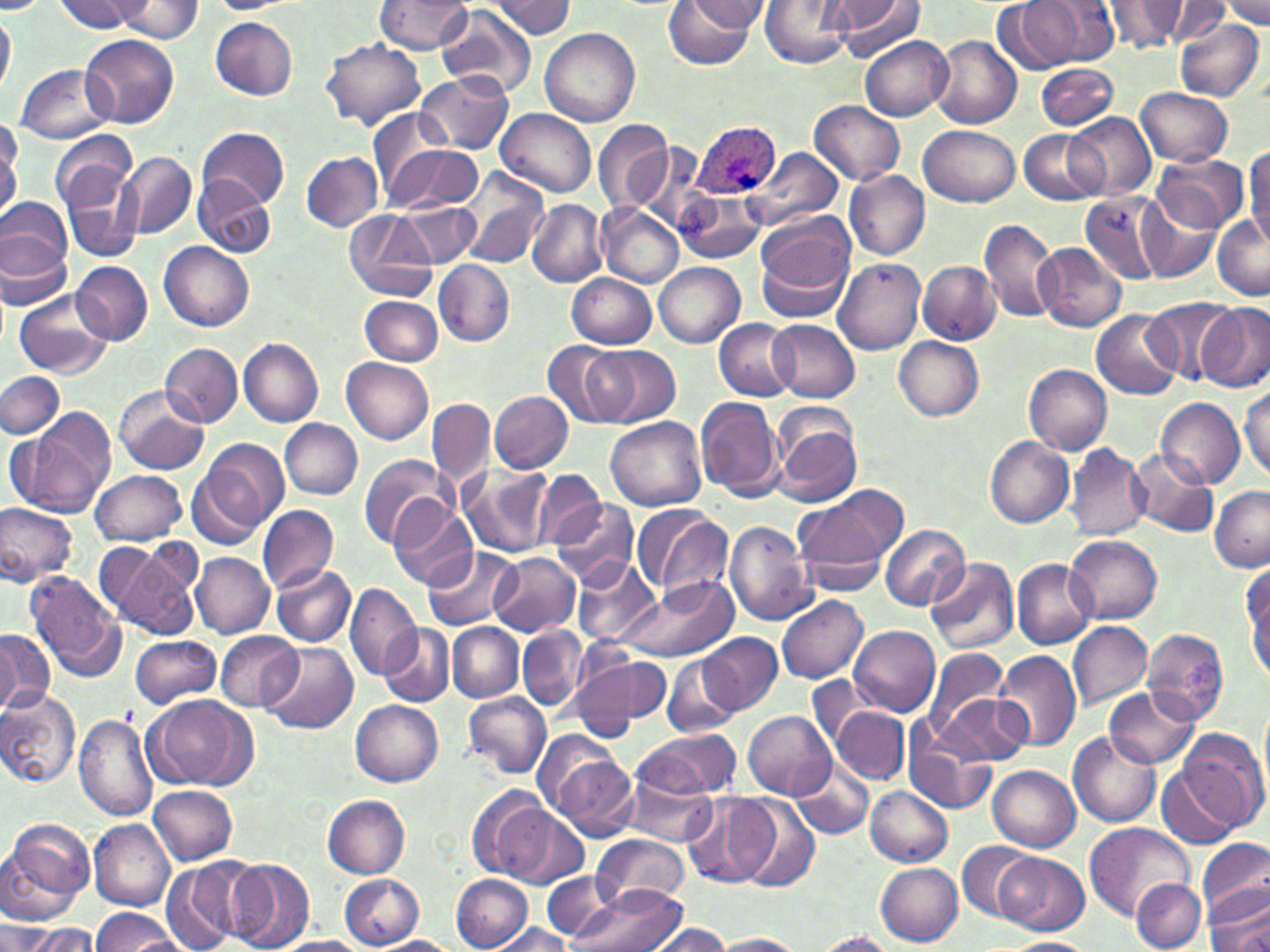

slide_level_diagnosis: Plasmodium ovale
uninfected_red_blood_cell_locations: 'approximate bounding boxes as [x1, y1, x2, y2] in pixels: [55, 0, 146, 33], [374, 0, 473, 55], [489, 0, 576, 38], [662, 0, 761, 69], [684, 0, 770, 31], [759, 0, 854, 69], [832, 0, 926, 62], [1032, 0, 1121, 65], [1175, 0, 1264, 38], [1220, 0, 1270, 29], [115, 1, 203, 43], [994, 1, 1089, 74], [1105, 1, 1187, 55], [1148, 1, 1229, 44], [0, 2, 48, 15], [205, 2, 293, 13], [438, 4, 537, 94], [0, 8, 15, 97], [210, 17, 297, 100], [1174, 19, 1264, 101], [540, 28, 640, 127], [80, 34, 179, 128], [931, 34, 1022, 130], [860, 37, 952, 120], [322, 38, 425, 130], [1037, 63, 1117, 129], [14, 64, 116, 144], [415, 72, 513, 154], [1134, 87, 1233, 166], [808, 100, 906, 186], [367, 107, 451, 201], [496, 108, 596, 197], [1068, 111, 1156, 199], [592, 120, 676, 212], [920, 124, 1020, 206], [199, 126, 290, 210], [1019, 130, 1109, 205], [50, 132, 138, 210], [629, 143, 709, 234], [385, 145, 484, 214], [0, 146, 18, 224], [747, 147, 845, 230], [1244, 147, 1269, 246], [118, 152, 196, 239], [300, 152, 383, 231], [1153, 152, 1248, 234], [59, 153, 144, 263], [456, 166, 549, 269], [843, 170, 929, 259], [193, 176, 275, 258], [673, 188, 766, 264], [1140, 191, 1224, 283], [1074, 192, 1167, 285], [1, 195, 72, 275], [527, 201, 606, 287], [597, 203, 684, 288], [403, 206, 478, 266], [342, 208, 438, 302], [1212, 214, 1269, 297], [754, 216, 857, 321], [979, 217, 1062, 324], [0, 226, 72, 309], [159, 242, 254, 331], [1035, 243, 1126, 332], [832, 258, 926, 355], [435, 260, 515, 347], [71, 261, 151, 345], [919, 261, 1001, 344], [654, 262, 744, 348], [567, 273, 656, 349], [14, 291, 114, 377], [360, 295, 441, 366], [1143, 298, 1239, 385], [1196, 302, 1268, 392], [1091, 309, 1181, 400], [714, 318, 798, 401], [769, 319, 859, 402], [894, 337, 984, 422], [239, 338, 323, 427], [541, 341, 638, 430], [161, 342, 242, 427], [591, 345, 680, 427], [342, 358, 433, 445], [1025, 364, 1113, 455], [0, 371, 66, 438], [1241, 385, 1270, 481], [115, 386, 209, 474], [489, 391, 574, 474], [696, 397, 784, 501], [1156, 397, 1244, 490], [427, 399, 495, 487], [15, 408, 116, 517], [771, 413, 860, 508], [606, 417, 707, 512], [280, 420, 363, 498], [984, 435, 1074, 528], [189, 440, 285, 546], [1065, 442, 1150, 541], [1128, 446, 1215, 537], [359, 452, 456, 550], [459, 465, 555, 557], [532, 468, 608, 548], [90, 470, 187, 547], [817, 484, 908, 566], [1208, 486, 1270, 572], [551, 495, 639, 585], [790, 495, 893, 592], [0, 501, 78, 586], [257, 503, 338, 593], [389, 503, 477, 592], [632, 503, 733, 601], [727, 520, 816, 625], [880, 525, 970, 613], [1064, 534, 1161, 625], [96, 542, 199, 642], [424, 545, 520, 630], [191, 553, 273, 639], [490, 553, 579, 637], [925, 555, 1019, 654], [572, 556, 661, 647], [1012, 558, 1097, 649], [272, 565, 355, 646], [1244, 565, 1270, 680], [26, 571, 128, 684], [619, 575, 737, 662], [345, 582, 419, 683], [777, 594, 868, 684], [448, 622, 523, 701], [1067, 622, 1152, 708], [379, 624, 454, 707], [849, 625, 940, 718], [519, 626, 587, 711], [1140, 628, 1230, 725], [0, 630, 51, 716], [214, 631, 303, 711], [699, 632, 780, 714], [131, 635, 222, 709], [259, 642, 357, 736], [922, 646, 1008, 737], [997, 650, 1081, 752], [663, 654, 742, 736], [574, 655, 664, 740], [807, 675, 878, 753], [1103, 686, 1199, 769], [0, 688, 83, 788], [940, 689, 1032, 766], [463, 691, 550, 779], [145, 694, 249, 791], [351, 701, 443, 786], [830, 704, 910, 784], [743, 710, 835, 799], [74, 715, 159, 822], [904, 717, 995, 816], [635, 727, 740, 798], [1175, 727, 1268, 835], [1069, 733, 1160, 829], [547, 746, 640, 841], [791, 760, 874, 842], [1158, 761, 1246, 850], [621, 766, 717, 848], [989, 766, 1080, 851], [865, 785, 952, 866], [150, 786, 237, 865], [467, 788, 556, 882], [681, 792, 771, 889], [323, 795, 411, 878], [731, 795, 821, 892], [493, 803, 589, 889], [88, 820, 175, 909], [0, 821, 91, 923], [1084, 823, 1193, 920], [591, 833, 689, 910], [1199, 837, 1270, 925], [957, 839, 1040, 923], [998, 853, 1090, 936], [159, 858, 257, 952], [227, 860, 314, 952], [877, 863, 963, 945], [544, 870, 621, 940], [339, 873, 425, 950], [451, 874, 532, 950], [1131, 878, 1205, 951], [1203, 882, 1270, 949], [565, 888, 687, 952], [92, 909, 177, 952], [3, 922, 62, 952], [18, 923, 100, 951], [491, 924, 570, 952], [646, 925, 733, 952], [811, 932, 894, 952], [711, 933, 804, 951], [373, 937, 459, 952], [1003, 937, 1095, 952], [275, 938, 370, 952]'
plasmodium_ovale_infected_red_blood_cell_locations: 'approximate bounding boxes as [x1, y1, x2, y2] in pixels: [691, 120, 782, 201]'
modality: optical microscopy
preparation: thin blood film
image_size: 1270×952 pixels
field_of_view: one of a larger specimen
magnification: 1000x
stain: May-Grünwald-Giemsa